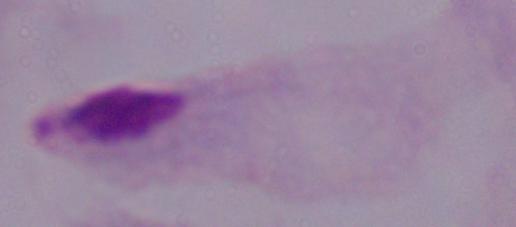

modality: micrograph
magnification: 1000x
identification: trichomonad